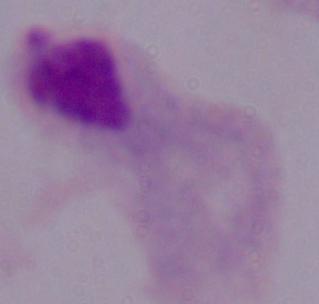
Photomicrograph. 1000x magnification. A trichomonad is shown.